Name the cell type shown.
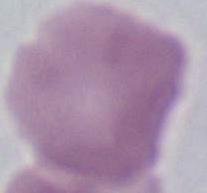
This is an erythrocyte.

Photomicrograph. 1000x magnification.